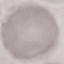

malaria status = uninfected
preparation = thin blood film
capture = smartphone through the microscope eyepiece
stain = Giemsa
image type = automatically extracted cell patch, resized to 64 × 64 pixels